Give the extent of all uninfected red blood cells.
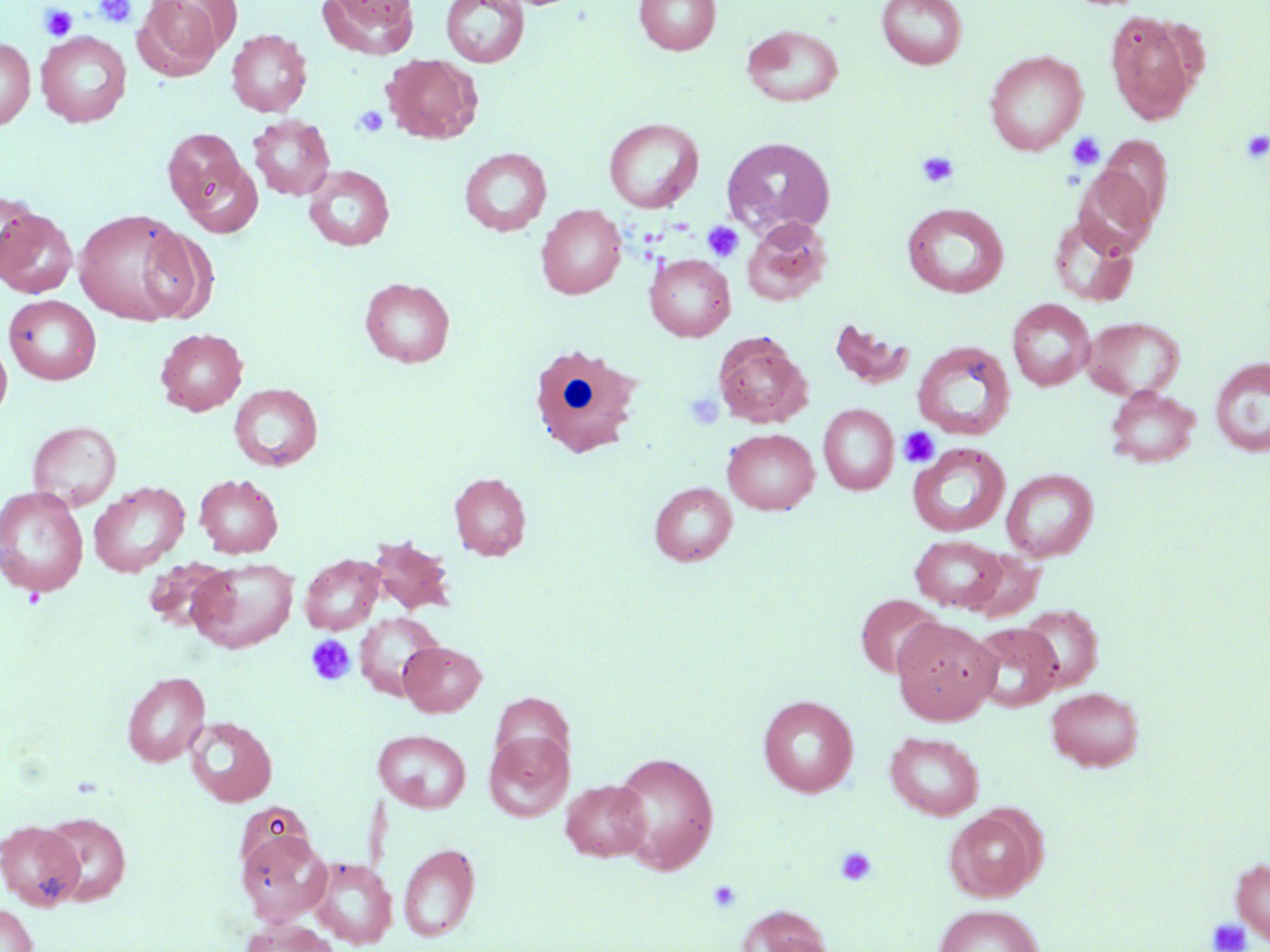
Approximate bounding boxes as [x1, y1, x2, y2] in pixels.
Uninfected red blood cells: [133, 0, 226, 80], [318, 0, 420, 59], [441, 0, 529, 68], [634, 0, 720, 55], [877, 0, 967, 69], [1105, 10, 1201, 125], [742, 24, 843, 107], [227, 29, 312, 117], [36, 31, 131, 127], [0, 37, 36, 130], [985, 50, 1088, 155], [383, 54, 483, 144], [248, 114, 335, 200], [604, 118, 703, 213], [162, 129, 246, 214], [1097, 136, 1173, 226], [721, 137, 836, 237], [459, 148, 551, 236], [178, 157, 263, 237], [303, 165, 395, 251], [1073, 167, 1159, 259], [1, 190, 41, 281], [902, 202, 1009, 298], [536, 204, 626, 299], [0, 207, 78, 298], [73, 208, 198, 326], [1048, 214, 1139, 307], [741, 216, 831, 306], [133, 226, 217, 323], [645, 254, 735, 341], [359, 277, 456, 367], [5, 295, 101, 384], [1007, 299, 1095, 390], [1082, 317, 1185, 400], [827, 318, 917, 391], [155, 328, 248, 415], [713, 332, 812, 428], [0, 336, 13, 423], [912, 340, 1016, 441], [1210, 356, 1270, 457], [229, 384, 323, 470], [1105, 385, 1200, 468], [819, 404, 899, 494], [27, 421, 122, 511], [723, 428, 819, 515], [908, 443, 1010, 537], [1001, 468, 1098, 562], [449, 472, 531, 560], [194, 474, 283, 558], [89, 481, 189, 576], [649, 482, 737, 566], [0, 485, 89, 597], [910, 535, 1008, 612], [368, 536, 456, 615], [963, 549, 1044, 622], [300, 554, 384, 634], [188, 558, 298, 653], [142, 559, 234, 635], [855, 593, 945, 680], [1018, 604, 1103, 692], [355, 612, 445, 700], [892, 617, 1000, 725], [970, 622, 1063, 712], [399, 641, 486, 716], [122, 671, 210, 766], [1046, 686, 1145, 771], [758, 695, 858, 797], [184, 716, 277, 807], [374, 729, 471, 812], [485, 730, 572, 821], [885, 731, 984, 820], [610, 751, 720, 874], [561, 779, 651, 861], [943, 805, 1045, 902], [39, 811, 131, 905], [0, 820, 85, 910], [236, 827, 331, 926], [399, 843, 480, 942], [307, 856, 397, 949], [1231, 857, 1270, 944], [0, 904, 38, 952], [933, 904, 1045, 952], [736, 907, 835, 952], [239, 918, 338, 952].

Platelet locations: [95, 0, 137, 28], [39, 4, 78, 41], [352, 106, 389, 137], [1241, 130, 1270, 163], [1067, 132, 1105, 170], [915, 152, 959, 189], [703, 220, 744, 261], [684, 391, 724, 430], [898, 426, 939, 467], [306, 634, 356, 686], [834, 845, 878, 886], [707, 879, 742, 914], [1206, 918, 1252, 952]. White blood cell locations: [527, 342, 643, 458]. Slide-level diagnosis: no evidence of blood parasites. Light microscopy. 1000x magnification. Image is 1270×952 pixels. May-Grünwald-Giemsa stain. Single field of view. Thin blood smear.